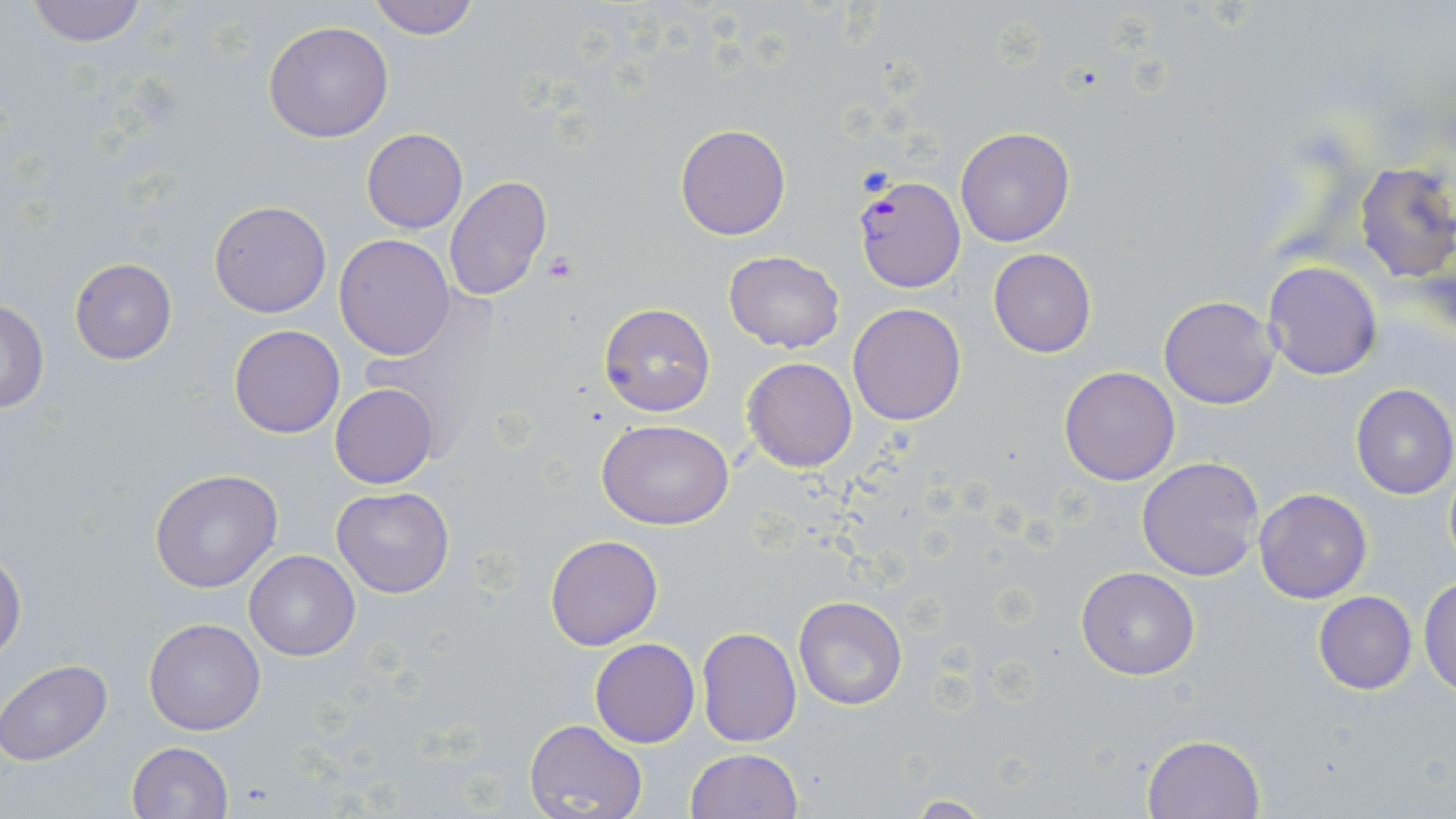 Approximate bounding boxes as [x1, y1, x2, y2] in pixels. Platelet locations: [544, 251, 579, 284]. Plasmodium falciparum-infected red blood cell locations: [853, 174, 965, 293]. Uninfected red blood cell locations: [22, 0, 151, 47], [367, 0, 480, 40], [263, 18, 394, 142], [675, 124, 789, 240], [954, 127, 1075, 248], [362, 128, 468, 233], [1353, 162, 1456, 283], [445, 176, 551, 301], [208, 201, 332, 318], [335, 234, 455, 359], [988, 248, 1096, 357], [722, 250, 844, 353], [70, 259, 177, 365], [1262, 261, 1383, 381], [1159, 294, 1279, 409], [0, 296, 49, 414], [599, 303, 715, 417], [847, 303, 966, 426], [228, 324, 346, 439], [743, 357, 857, 472], [1059, 365, 1181, 485], [330, 383, 439, 489], [1350, 384, 1456, 500], [597, 420, 732, 530], [1137, 456, 1266, 581], [1444, 464, 1456, 576], [149, 468, 283, 593], [332, 487, 455, 598], [1254, 489, 1371, 604], [545, 535, 663, 650], [243, 550, 360, 660], [0, 551, 25, 660], [1076, 566, 1200, 679], [1420, 576, 1456, 698], [1313, 591, 1417, 694], [794, 597, 907, 710], [143, 617, 266, 735], [696, 626, 801, 747], [589, 638, 699, 748], [0, 658, 113, 766], [524, 718, 648, 819], [1141, 732, 1266, 819], [126, 741, 234, 819], [685, 748, 801, 819], [904, 796, 992, 817]. Slide-level diagnosis: Plasmodium falciparum. Thin blood film. 1000x magnification. Light microscopy. May-Grünwald-Giemsa-stained preparation. Single field of view. Image is 1456×819 pixels.